Locate every blood parasite and identify its species.
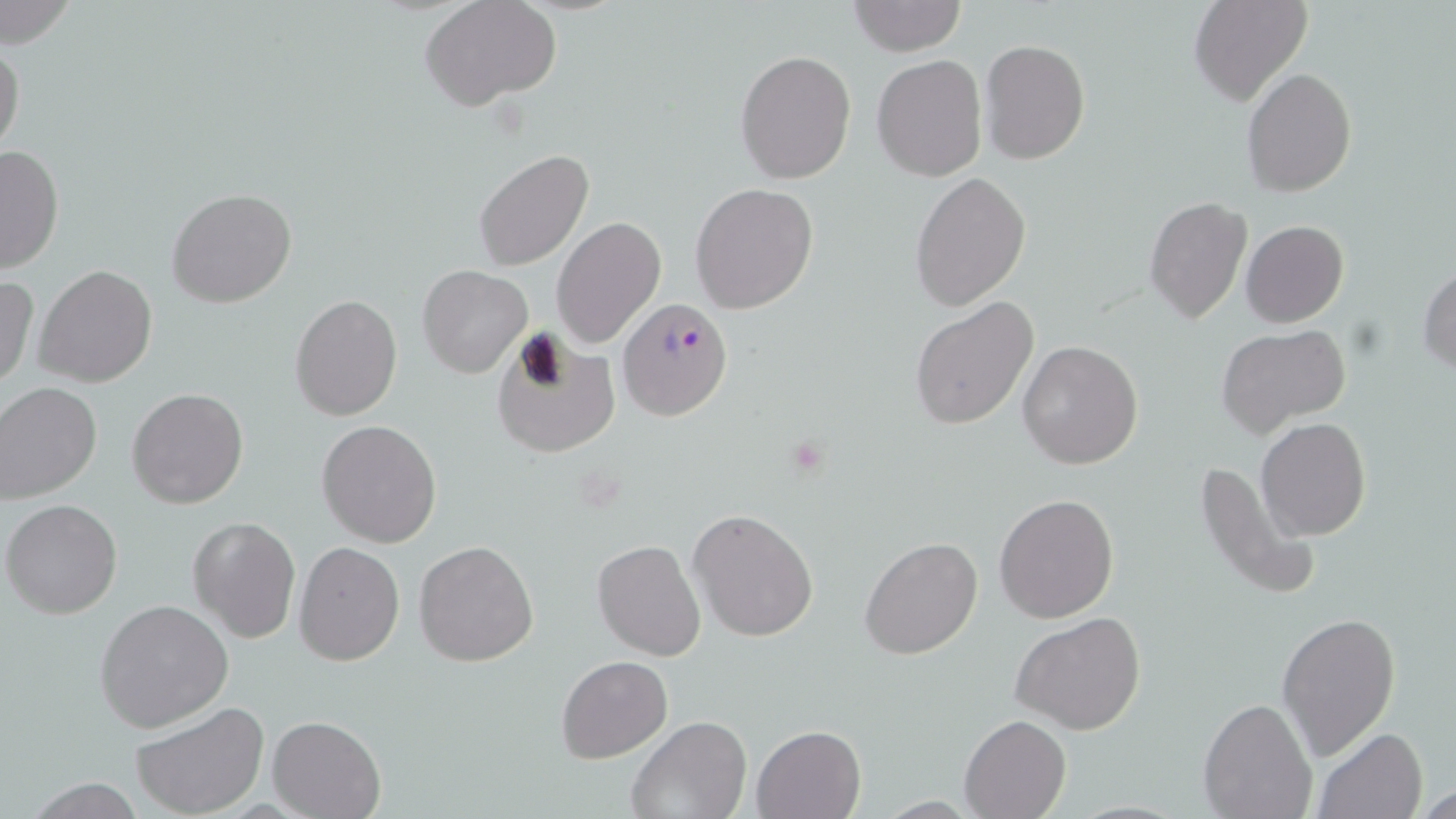

Approximate bounding boxes as (x1, y1, x2, y2) in pixels.
Plasmodium falciparum-infected red blood cells: (620, 298, 731, 420).
No Plasmodium ovale, Plasmodium malariae, Plasmodium vivax, Babesia divergens, or Trypanosoma brucei observed.

slide-level diagnosis = Plasmodium falciparum
field of view = single
preparation = thin blood film
uninfected red blood cell locations = approximate bounding boxes as (x1, y1, x2, y2) in pixels: (0, 0, 77, 50), (422, 0, 563, 112), (1187, 0, 1312, 107), (849, 1, 965, 55), (980, 39, 1091, 164), (0, 40, 23, 155), (735, 49, 855, 183), (871, 55, 987, 181), (1242, 69, 1357, 196), (0, 145, 64, 275), (474, 149, 595, 273), (910, 173, 1030, 309), (690, 183, 819, 315), (167, 188, 296, 308), (1143, 196, 1252, 324), (552, 216, 667, 351), (1241, 220, 1350, 328), (34, 264, 158, 388), (1418, 264, 1456, 375), (418, 265, 532, 378), (0, 273, 39, 389), (288, 295, 403, 421), (910, 296, 1040, 431), (1214, 323, 1352, 437), (490, 332, 620, 458), (1017, 340, 1144, 470), (0, 384, 101, 504), (127, 389, 248, 510), (1255, 417, 1371, 541), (317, 419, 441, 547), (1194, 457, 1323, 603), (994, 493, 1120, 624), (3, 499, 123, 619), (688, 509, 818, 642), (187, 517, 299, 644), (860, 537, 982, 659), (414, 539, 539, 667), (592, 540, 706, 660), (293, 541, 406, 665), (95, 599, 233, 733), (1011, 611, 1147, 735), (1276, 612, 1403, 760), (557, 655, 672, 762), (1197, 697, 1318, 819), (132, 701, 268, 817), (958, 715, 1071, 819), (267, 716, 385, 819), (625, 716, 750, 819), (751, 723, 867, 818), (1312, 729, 1427, 818), (21, 777, 151, 817), (1417, 784, 1456, 817)
image size = 1456×819 pixels
stain = May-Grünwald-Giemsa
magnification = 1000x
modality = optical microscopy